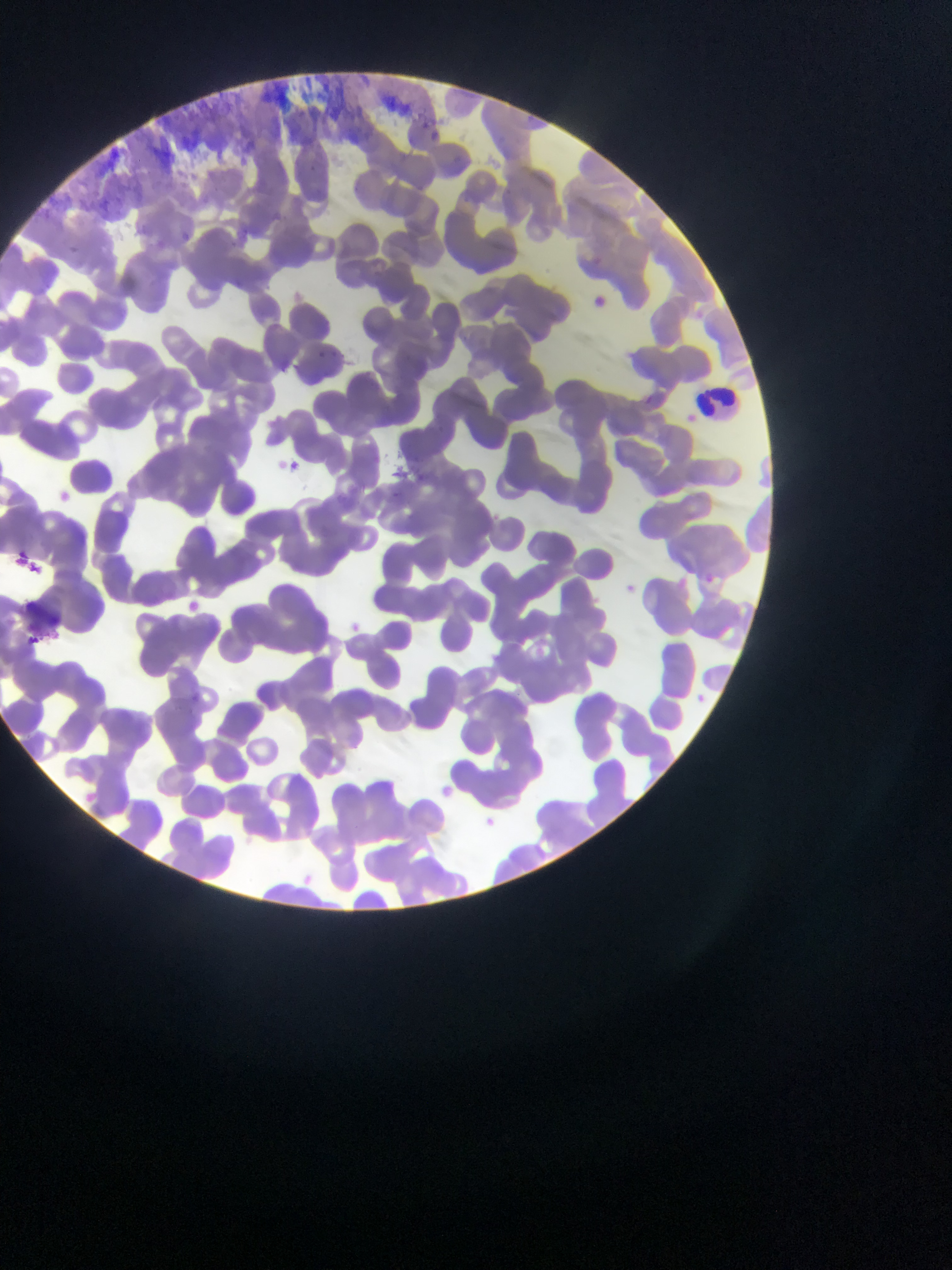
Approximate bounding boxes as {left, top, right, bottom} in pixels. Malaria parasite locations: {428, 129, 445, 144}, {593, 292, 608, 310}, {316, 345, 343, 363}, {286, 457, 302, 472}, {54, 487, 71, 505}, {678, 570, 694, 590}, {704, 571, 721, 586}, {622, 579, 641, 601}, {186, 596, 206, 614}, {348, 618, 365, 635}, {24, 628, 46, 646}, {694, 689, 709, 706}, {443, 780, 460, 798}, {479, 810, 500, 828}. Leukocyte locations: {697, 382, 740, 427}. Collected in Ghana. Thin blood film. Mobile-phone photograph taken through the microscope. Image is 952×1270 pixels. Single field of view.